Identify the cell.
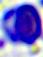
A leukocyte.

Photomicrograph. Captured at 400x magnification.